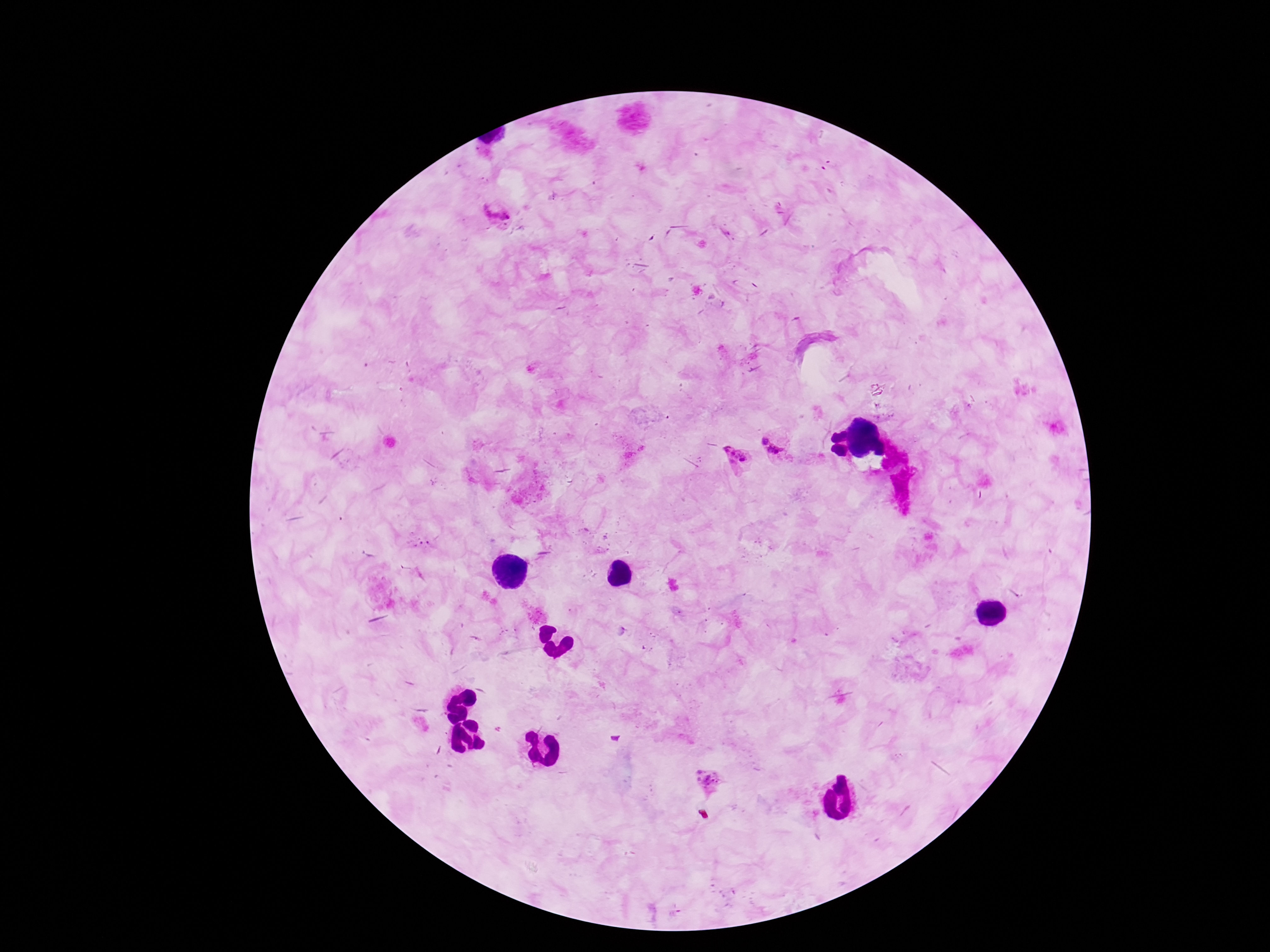
Plasmodium parasite locations = approximate centers as [x, y] in pixels: [495, 211], [764, 439], [775, 451], [735, 457], [425, 546], [498, 729], [711, 780]
patient malaria status = infected
magnification = 100x
image size = 1270×952 pixels
capture = smartphone camera through the microscope eyepiece
field of view = single
preparation = thick blood film
stain = Giemsa